Assess this cell for malaria.
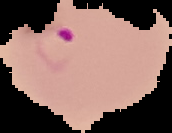
It is parasitized.

The area outside the segmented cell region is set to black. From a thin blood smear. Image is 172×133 pixels.